State the preparation type.
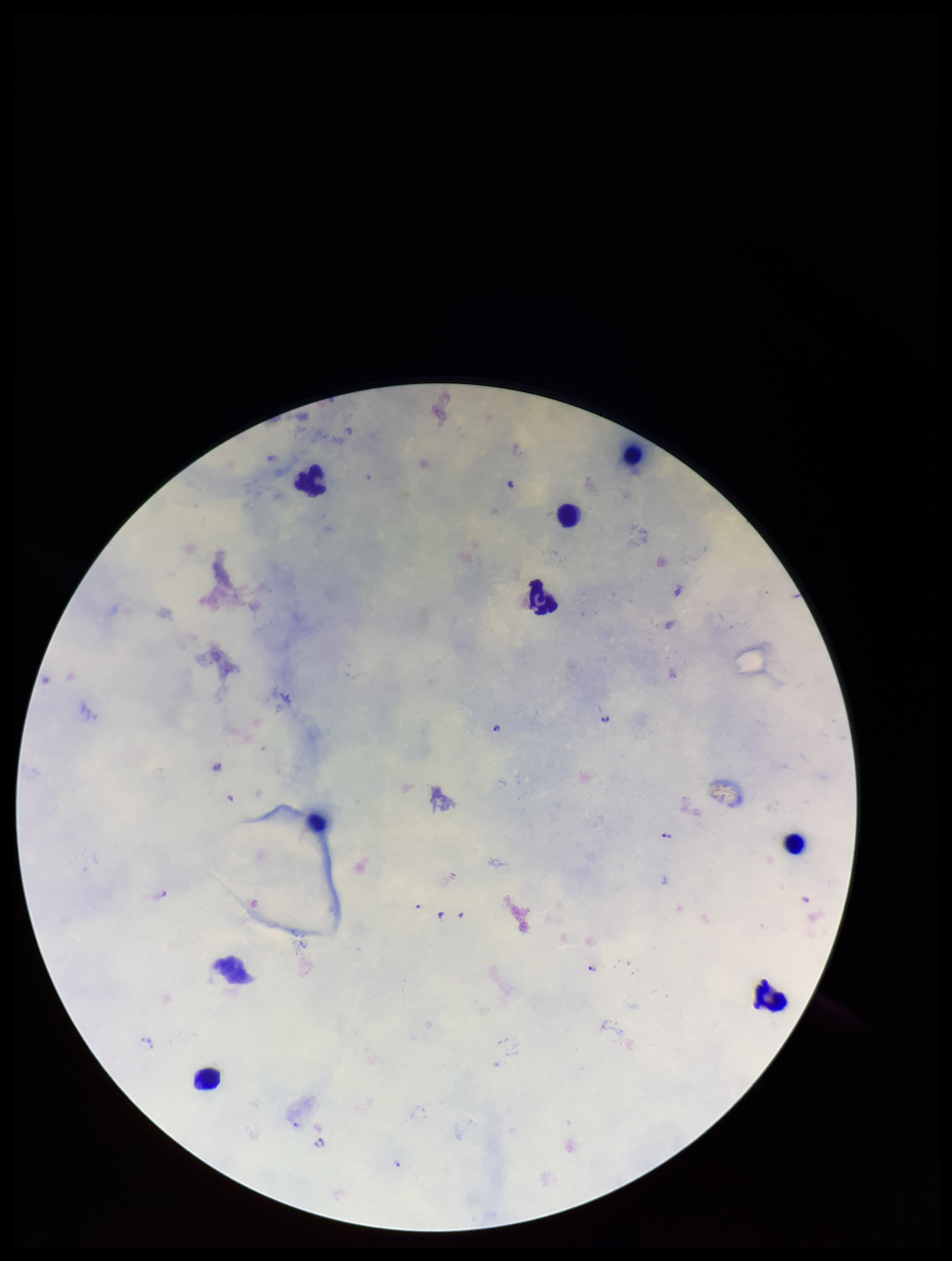
It is a thick blood smear.

Species reported for this patient: Plasmodium falciparum. Plasmodium parasites: seen. Single field of view. Stained with Giemsa. Leukocyte count: 8. Image is 952×1261 pixels. Patient malaria status: infected. Parasite count: 9. Photographed through the microscope eyepiece with a smartphone camera.